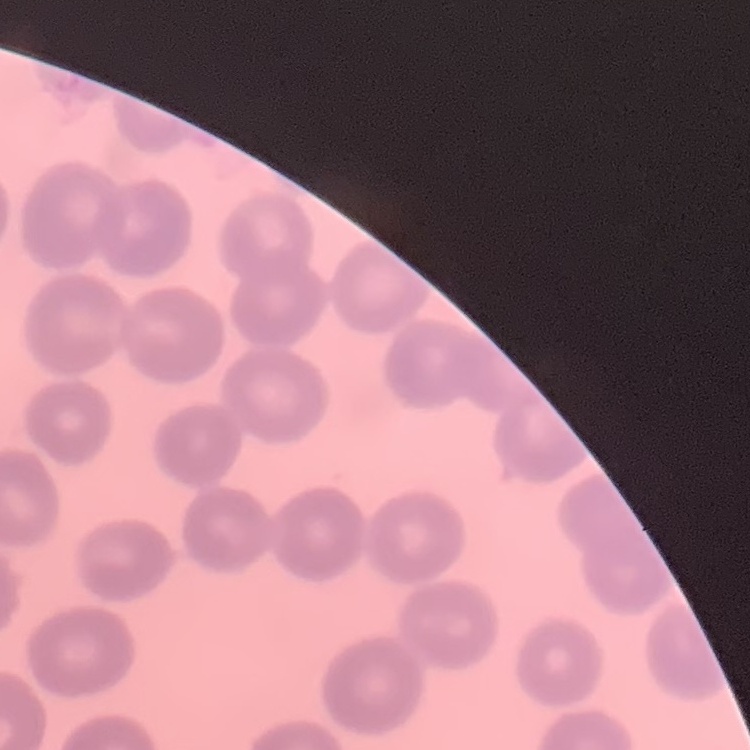

red blood cell morphology = no rouleaux formation
preparation = thin blood film
image type = one tile cut from a larger photomicrograph
stain = Field's or Giemsa